Outline each Plasmodium parasite.
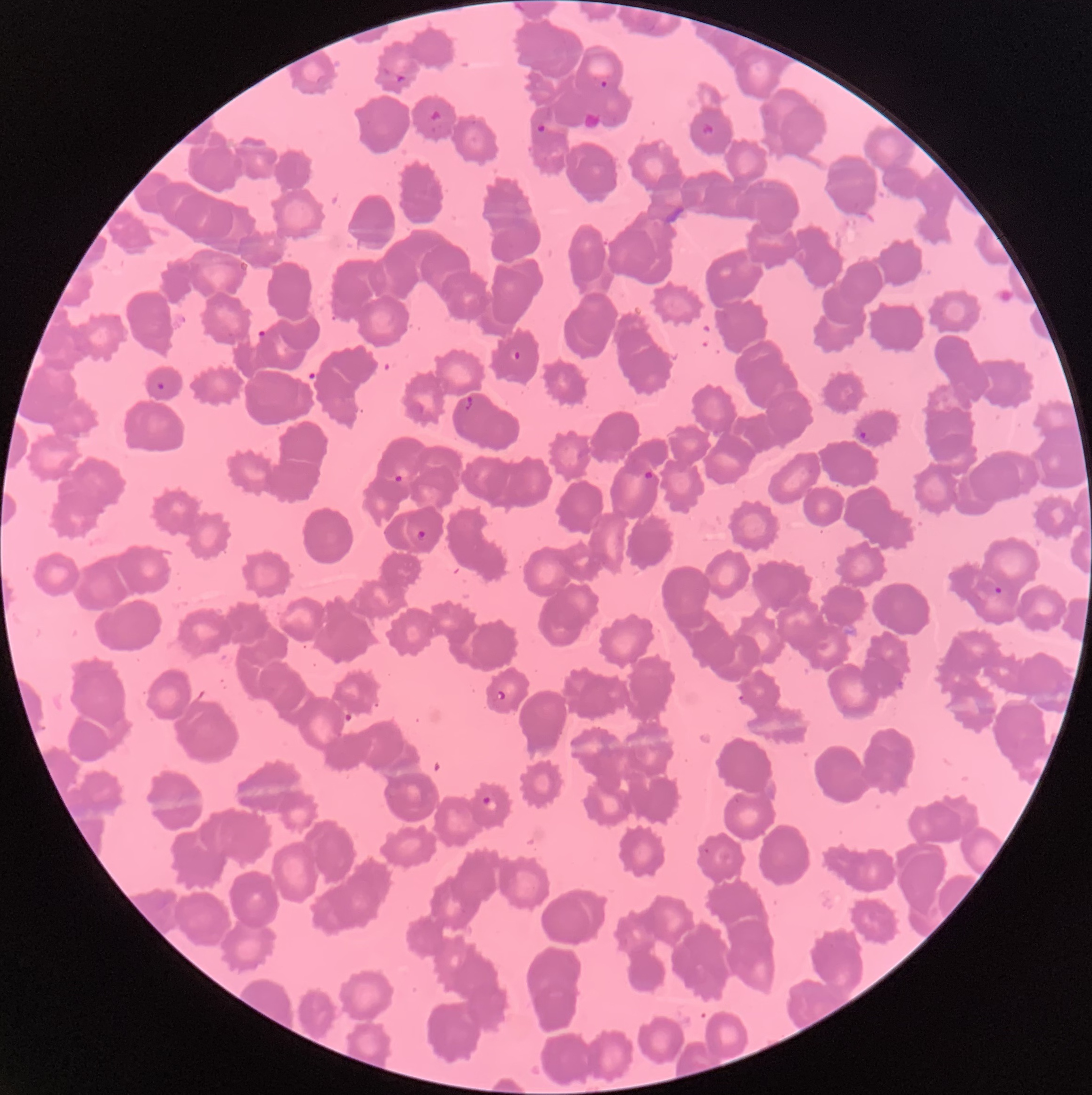

Approximate bounding boxes as (x1, y1, x2, y2) in pixels.
Plasmodium parasites: (381, 65, 408, 83), (594, 77, 614, 93), (428, 109, 446, 135), (700, 123, 714, 135), (509, 348, 522, 362), (156, 381, 165, 390), (463, 395, 473, 410), (857, 430, 874, 443), (643, 469, 659, 487), (392, 473, 404, 484), (415, 530, 428, 541), (994, 585, 1003, 595), (488, 690, 505, 704), (737, 694, 747, 701), (481, 797, 498, 812).

The red blood cells show rouleaux formation. Optical microscopy. Thin blood smear. Image is 1092×1095 pixels.